Report the malaria status of this cell.
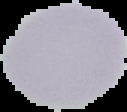
Uninfected.

image type = segmented cell region on a black background
preparation = thin blood film
image size = 127×112 pixels